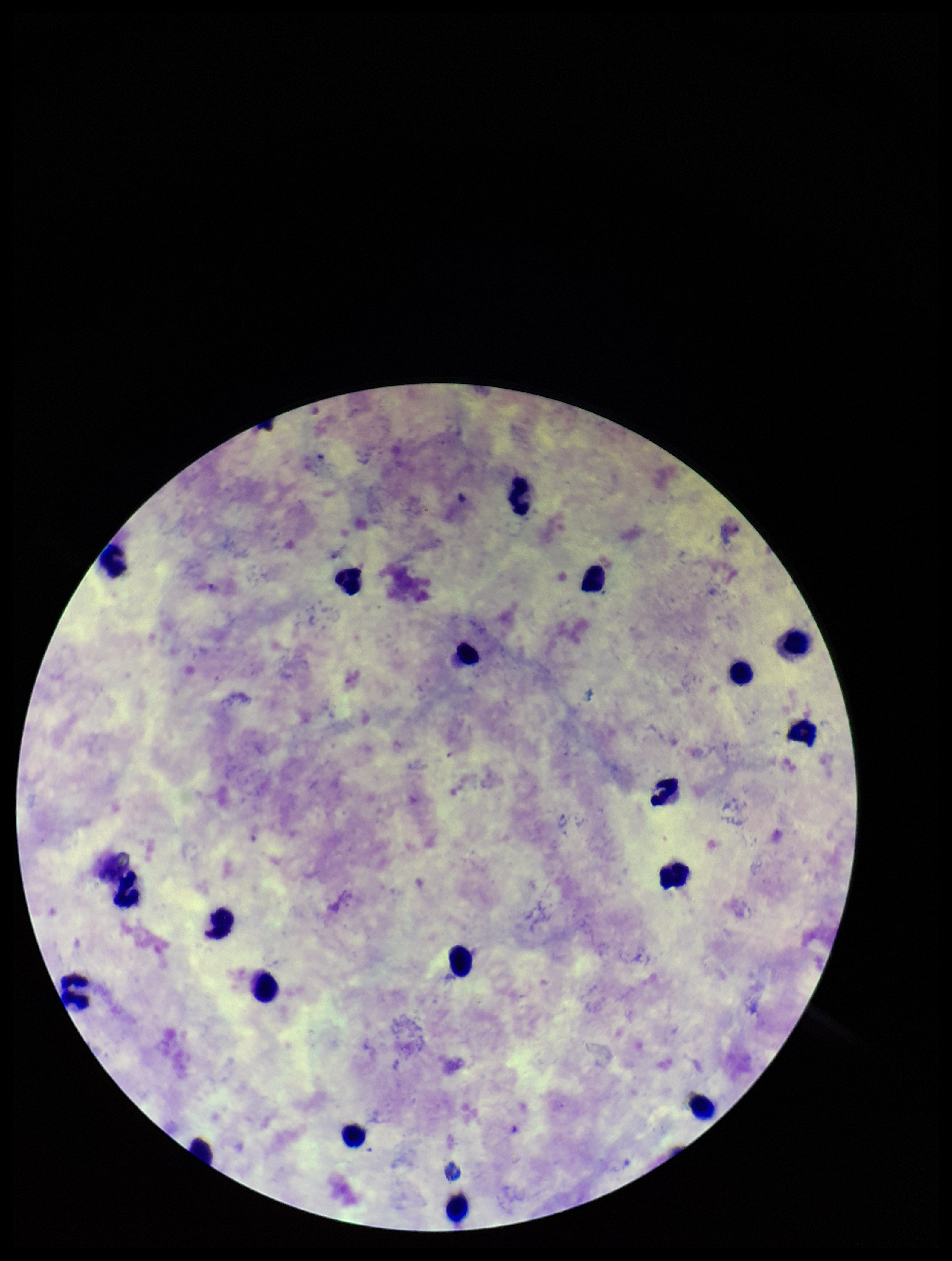
Summary:
  - Patient malaria status: infected
  - Species reported for this patient: Plasmodium vivax
  - Parasite count: 0
  - Field of view: one from this slide
  - Plasmodium parasites: none seen
  - Capture: smartphone photograph through the microscope eyepiece
  - Stain: Giemsa
  - Image size: 952×1261 pixels
  - Leukocyte count: 18
  - Preparation: thick smear